Outline each Plasmodium ovale-infected red blood cell.
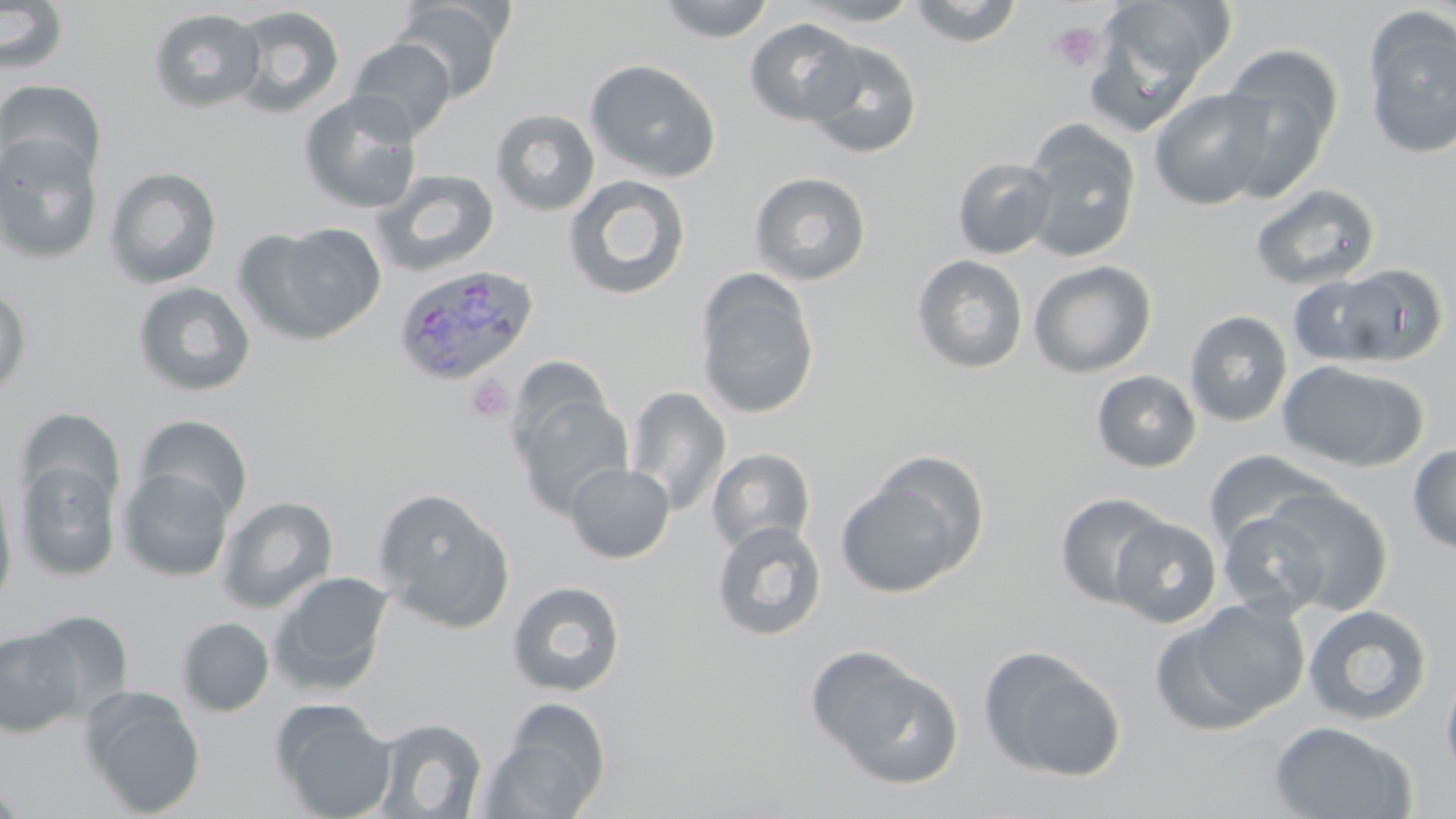
Approximate bounding boxes as (x1,y1)-(x2,y2) corner pairs in pixels.
Plasmodium ovale-infected red blood cells: (392,264)-(540,387).

slide-level diagnosis = Plasmodium ovale
uninfected red blood cell locations = approximate bounding boxes as (x1,y1)-(x2,y2) corner pairs in pixels: (394,0)-(509,102), (656,0)-(776,42), (790,0)-(924,27), (906,0)-(1025,47), (1087,0)-(1227,121), (0,2)-(70,76), (226,5)-(346,118), (148,8)-(265,113), (1361,10)-(1456,161), (744,18)-(865,126), (348,38)-(456,142), (802,40)-(922,159), (1219,45)-(1343,199), (584,59)-(722,182), (0,78)-(107,181), (1149,88)-(1274,211), (298,91)-(423,214), (490,109)-(600,216), (1022,124)-(1141,263), (0,132)-(103,265), (952,157)-(1057,259), (104,167)-(223,289), (371,168)-(500,277), (749,172)-(872,285), (563,175)-(691,301), (1250,183)-(1380,291), (238,223)-(387,347), (912,254)-(1029,374), (1028,260)-(1157,378), (1337,263)-(1448,365), (695,268)-(820,420), (1287,274)-(1396,366), (132,281)-(257,397), (0,287)-(31,399), (1184,310)-(1293,428), (1276,360)-(1428,472), (1091,370)-(1202,473), (623,385)-(732,515), (512,391)-(633,518), (14,408)-(124,514), (135,415)-(253,523), (1407,443)-(1456,554), (707,448)-(816,554), (1203,450)-(1335,550), (16,456)-(122,581), (564,462)-(675,563), (119,468)-(233,581), (834,469)-(982,599), (0,474)-(17,615), (1254,486)-(1394,614), (372,487)-(515,634), (1054,492)-(1173,608), (217,495)-(338,614), (1216,509)-(1335,619), (1109,517)-(1222,627), (711,519)-(827,641), (269,570)-(394,696), (507,580)-(626,697), (1157,599)-(1311,732), (1302,604)-(1432,726), (29,609)-(134,720), (176,617)-(275,716), (0,628)-(85,737), (978,645)-(1128,783), (811,651)-(965,789), (1440,667)-(1456,785), (80,687)-(206,817), (481,699)-(612,818), (274,703)-(396,819), (371,717)-(487,818), (1268,720)-(1417,819), (0,778)-(28,819)
stain = May-Grünwald-Giemsa
modality = light microscopy
magnification = 1000x
preparation = thin blood film
field of view = one of a larger specimen
image size = 1456×819 pixels
platelet locations = approximate bounding boxes as (x1,y1)-(x2,y2) corner pairs in pixels: (1046,21)-(1104,74), (467,377)-(513,422)